State the blood parasite species.
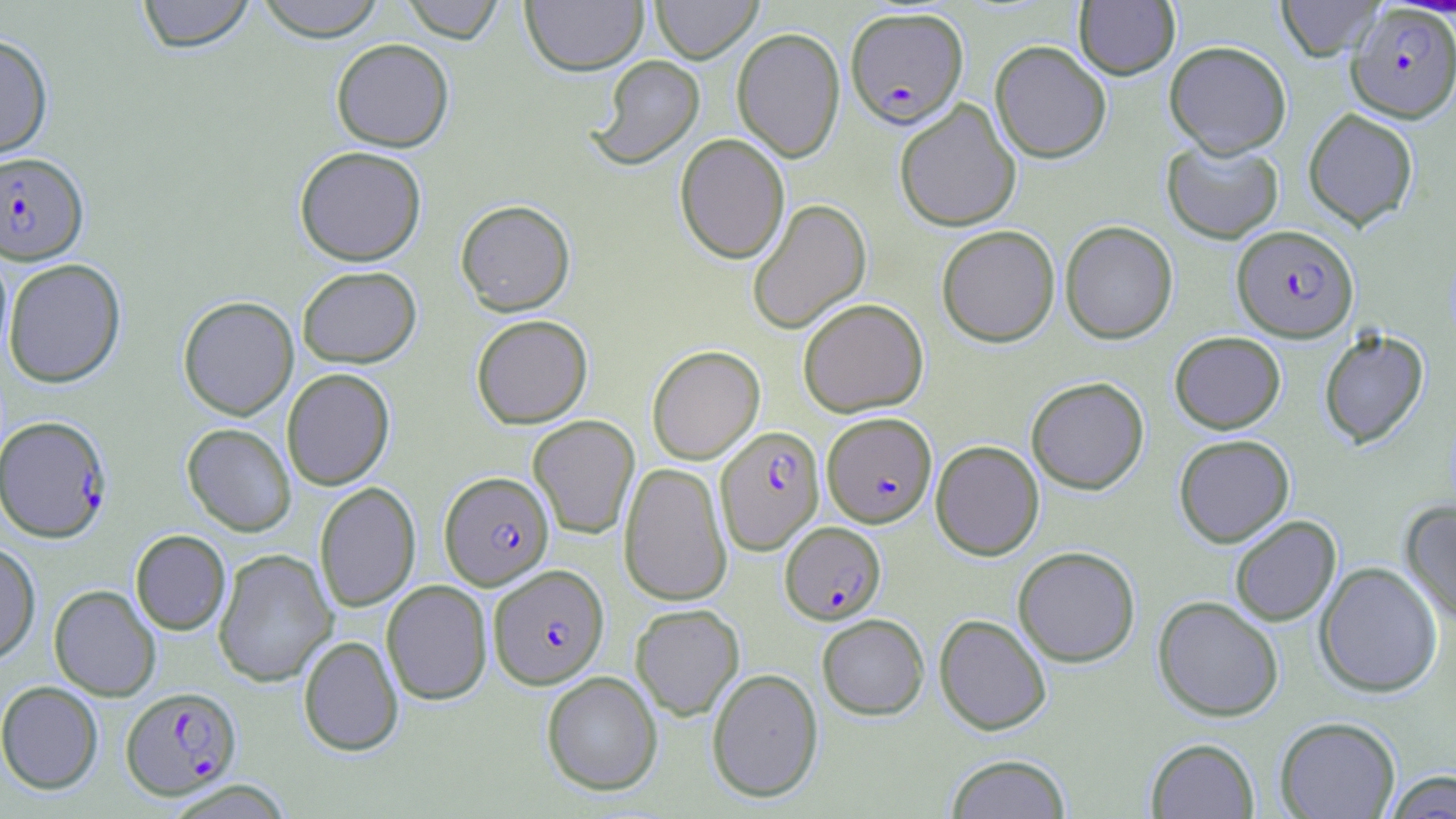

Plasmodium falciparum.

Summary:
  - Coordinate format: approximate bounding boxes as named x1/y1/x2/y2 corners in pixels
  - Uninfected red blood cell locations: (x1=136, y1=0, x2=255, y2=53), (x1=254, y1=0, x2=387, y2=41), (x1=398, y1=0, x2=505, y2=43), (x1=520, y1=0, x2=648, y2=75), (x1=651, y1=0, x2=762, y2=63), (x1=1276, y1=0, x2=1384, y2=61), (x1=1074, y1=1, x2=1180, y2=79), (x1=731, y1=27, x2=845, y2=162), (x1=0, y1=33, x2=53, y2=159), (x1=331, y1=38, x2=454, y2=152), (x1=990, y1=40, x2=1112, y2=163), (x1=1164, y1=40, x2=1291, y2=157), (x1=590, y1=55, x2=705, y2=170), (x1=894, y1=99, x2=1022, y2=232), (x1=1303, y1=108, x2=1419, y2=230), (x1=675, y1=133, x2=790, y2=263), (x1=1162, y1=138, x2=1284, y2=244), (x1=294, y1=145, x2=426, y2=266), (x1=747, y1=198, x2=872, y2=334), (x1=456, y1=199, x2=575, y2=315), (x1=1060, y1=220, x2=1178, y2=344), (x1=936, y1=224, x2=1059, y2=347), (x1=3, y1=258, x2=126, y2=388), (x1=297, y1=266, x2=421, y2=367), (x1=178, y1=295, x2=299, y2=420), (x1=798, y1=298, x2=928, y2=417), (x1=471, y1=314, x2=593, y2=429), (x1=1318, y1=328, x2=1429, y2=449), (x1=1169, y1=331, x2=1285, y2=434), (x1=646, y1=345, x2=765, y2=464), (x1=281, y1=368, x2=395, y2=490), (x1=1026, y1=376, x2=1149, y2=494), (x1=528, y1=415, x2=640, y2=539), (x1=182, y1=423, x2=296, y2=536), (x1=1174, y1=434, x2=1294, y2=547), (x1=930, y1=440, x2=1044, y2=560), (x1=619, y1=461, x2=732, y2=605), (x1=315, y1=482, x2=421, y2=612), (x1=1400, y1=502, x2=1456, y2=625), (x1=1229, y1=515, x2=1341, y2=626), (x1=130, y1=529, x2=231, y2=635), (x1=0, y1=541, x2=40, y2=664), (x1=1013, y1=546, x2=1140, y2=667), (x1=213, y1=548, x2=337, y2=687), (x1=1315, y1=561, x2=1443, y2=697), (x1=382, y1=579, x2=492, y2=705), (x1=49, y1=584, x2=161, y2=701), (x1=1153, y1=595, x2=1284, y2=722), (x1=630, y1=603, x2=745, y2=720), (x1=816, y1=613, x2=930, y2=720), (x1=934, y1=614, x2=1052, y2=735), (x1=298, y1=635, x2=404, y2=756), (x1=707, y1=667, x2=823, y2=803), (x1=541, y1=671, x2=663, y2=796), (x1=0, y1=680, x2=103, y2=794), (x1=1275, y1=716, x2=1401, y2=818), (x1=1145, y1=737, x2=1260, y2=818), (x1=945, y1=753, x2=1072, y2=819), (x1=1383, y1=770, x2=1456, y2=818)
  - Plasmodium falciparum-infected red blood cell locations: (x1=1347, y1=4, x2=1456, y2=122), (x1=845, y1=6, x2=968, y2=127), (x1=0, y1=152, x2=88, y2=264), (x1=1232, y1=224, x2=1358, y2=342), (x1=822, y1=412, x2=937, y2=527), (x1=0, y1=415, x2=113, y2=542), (x1=715, y1=425, x2=825, y2=554), (x1=440, y1=471, x2=554, y2=589), (x1=780, y1=521, x2=886, y2=624), (x1=489, y1=564, x2=609, y2=689), (x1=121, y1=686, x2=241, y2=799)
  - Field of view: single
  - Magnification: 1000x
  - Preparation: thin blood film
  - Image size: 1456×819 pixels
  - Modality: light microscopy
  - Stain: May-Grünwald-Giemsa